Point out each malaria parasite and each leukocyte.
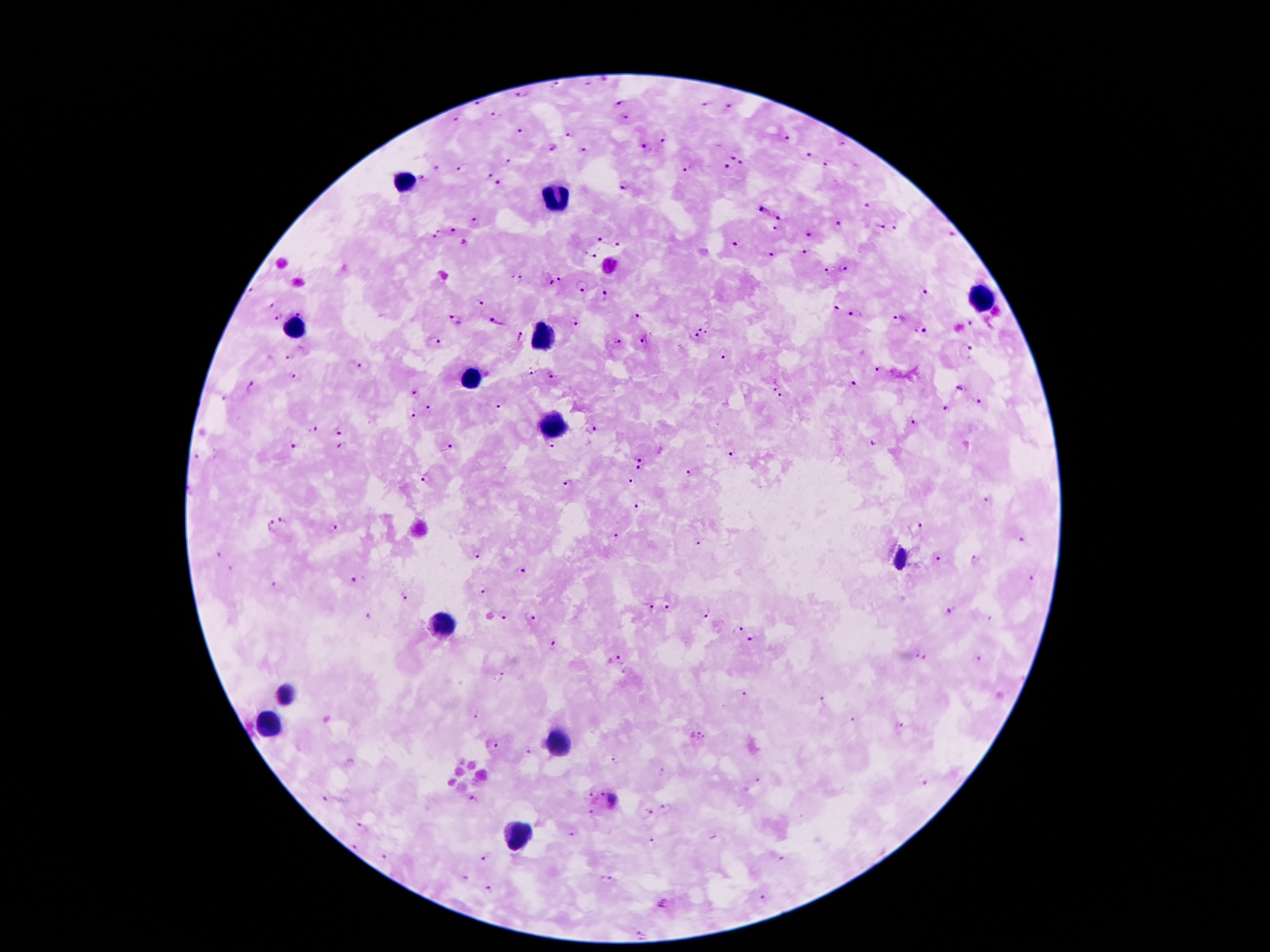

Approximate object centers, in pixels from the top-left corner.
Malaria parasites: (x=556, y=85), (x=521, y=95), (x=479, y=103), (x=621, y=104), (x=705, y=104), (x=728, y=105), (x=496, y=115), (x=625, y=117), (x=458, y=120), (x=520, y=130), (x=569, y=133), (x=785, y=137), (x=664, y=138), (x=843, y=146), (x=554, y=148), (x=643, y=148), (x=585, y=151), (x=809, y=156), (x=731, y=158), (x=509, y=160), (x=744, y=163), (x=830, y=163), (x=436, y=167), (x=691, y=167), (x=463, y=168), (x=726, y=168), (x=490, y=175), (x=424, y=179), (x=625, y=184), (x=499, y=186), (x=866, y=205), (x=764, y=211), (x=781, y=216), (x=474, y=221), (x=839, y=224), (x=777, y=227), (x=880, y=227), (x=452, y=229), (x=895, y=229), (x=436, y=233), (x=809, y=234), (x=950, y=236), (x=600, y=239), (x=466, y=242), (x=618, y=244), (x=736, y=245), (x=806, y=251), (x=594, y=255), (x=772, y=255), (x=845, y=270), (x=828, y=271), (x=517, y=278), (x=560, y=279), (x=550, y=283), (x=583, y=285), (x=251, y=290), (x=925, y=293), (x=605, y=296), (x=480, y=302), (x=271, y=304), (x=836, y=309), (x=301, y=311), (x=856, y=316), (x=278, y=317), (x=456, y=317), (x=638, y=320), (x=574, y=321), (x=897, y=321), (x=497, y=323), (x=972, y=325), (x=704, y=326), (x=921, y=331), (x=520, y=335), (x=695, y=337), (x=645, y=340), (x=435, y=342), (x=617, y=342), (x=966, y=351), (x=724, y=355), (x=288, y=356), (x=362, y=364), (x=878, y=370), (x=532, y=371), (x=551, y=375), (x=296, y=376), (x=854, y=385), (x=773, y=387), (x=253, y=390), (x=961, y=390), (x=415, y=395), (x=781, y=397), (x=501, y=402), (x=976, y=402), (x=429, y=408), (x=947, y=409), (x=413, y=414), (x=915, y=422), (x=317, y=429), (x=340, y=430), (x=592, y=430), (x=873, y=444), (x=296, y=446), (x=448, y=447), (x=550, y=447), (x=343, y=448), (x=732, y=454), (x=639, y=456), (x=639, y=468), (x=690, y=472), (x=424, y=477), (x=630, y=482), (x=567, y=485), (x=986, y=500), (x=639, y=506), (x=284, y=519), (x=918, y=524), (x=270, y=526), (x=332, y=529), (x=613, y=535), (x=1024, y=539), (x=695, y=543), (x=475, y=554), (x=219, y=555), (x=938, y=559), (x=976, y=561), (x=231, y=569), (x=521, y=571), (x=355, y=578), (x=1033, y=579), (x=274, y=586), (x=484, y=591), (x=407, y=596), (x=668, y=607), (x=651, y=608), (x=945, y=609), (x=704, y=613), (x=367, y=616), (x=530, y=617), (x=503, y=618), (x=988, y=619), (x=739, y=631), (x=750, y=640), (x=555, y=645), (x=920, y=656), (x=622, y=657), (x=980, y=661), (x=500, y=677), (x=742, y=694), (x=820, y=700), (x=474, y=718), (x=852, y=719), (x=901, y=725), (x=702, y=735), (x=496, y=744), (x=529, y=752), (x=615, y=758), (x=758, y=780), (x=924, y=782), (x=600, y=793), (x=590, y=795), (x=326, y=797), (x=473, y=798), (x=614, y=798), (x=664, y=807), (x=648, y=813), (x=591, y=814), (x=362, y=826), (x=572, y=833), (x=652, y=841), (x=356, y=847), (x=385, y=856), (x=484, y=857), (x=611, y=878), (x=464, y=879), (x=488, y=890), (x=763, y=900), (x=662, y=905), (x=639, y=934).
Leukocytes: (x=401, y=184), (x=557, y=195), (x=979, y=298), (x=294, y=330), (x=541, y=333), (x=470, y=375), (x=549, y=427), (x=900, y=557), (x=440, y=624), (x=284, y=693), (x=267, y=721), (x=556, y=743), (x=512, y=839).

100x magnification. Patient malaria status: infected with Plasmodium falciparum. Image is 1270×952 pixels. One field from this slide. Photographed through the microscope eyepiece with a smartphone camera. Giemsa stain. Thick blood smear.